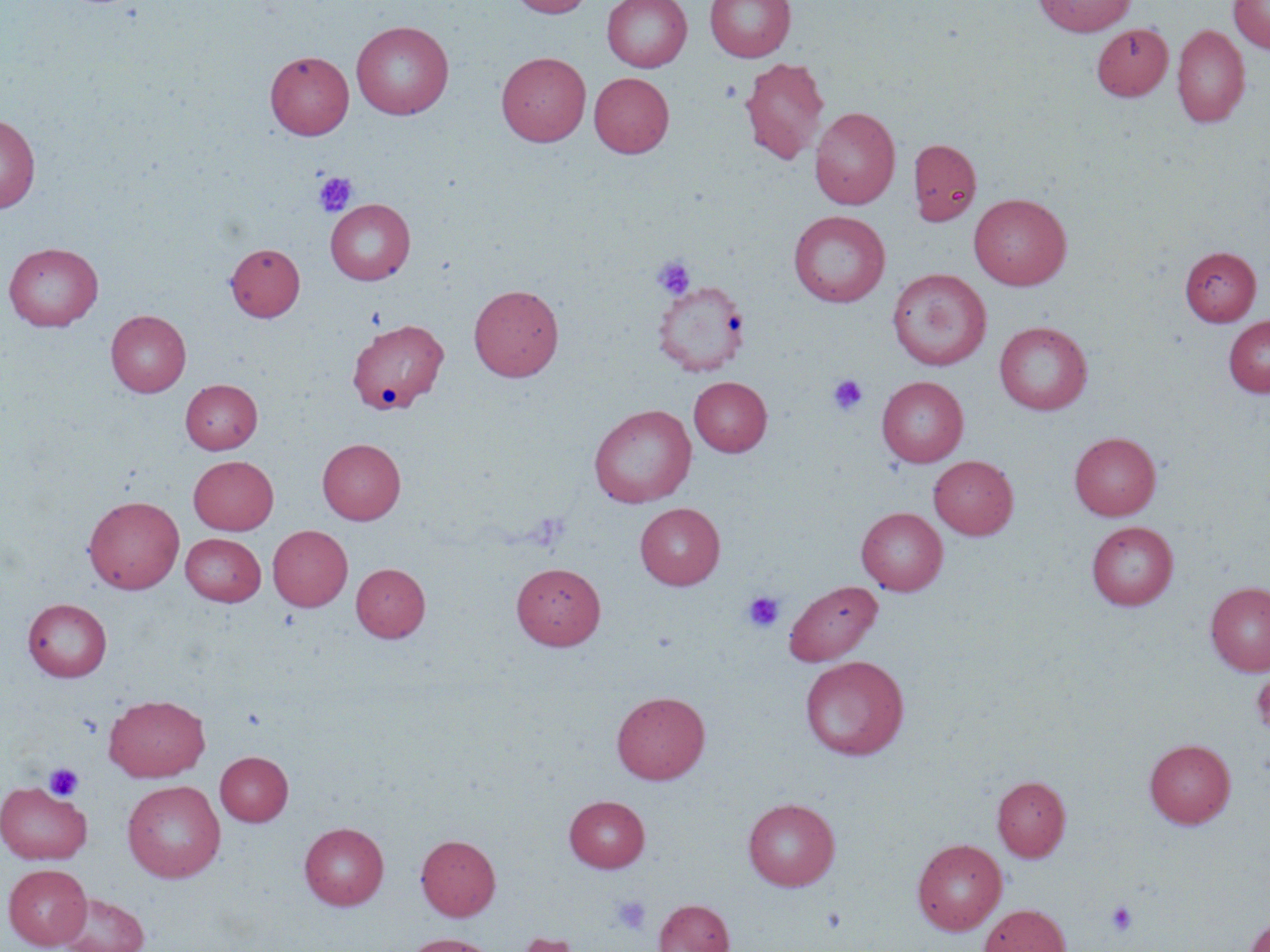

Summary:
  - Coordinate format: approximate bounding boxes as [x1, y1, x2, y2] in pixels
  - Uninfected red blood cell locations: [509, 0, 594, 17], [602, 0, 692, 72], [705, 0, 795, 62], [1035, 0, 1135, 36], [1228, 0, 1270, 53], [351, 20, 454, 118], [1092, 23, 1173, 101], [1172, 25, 1249, 127], [265, 51, 354, 139], [496, 51, 591, 146], [740, 57, 830, 164], [497, 68, 674, 153], [589, 72, 674, 158], [810, 107, 900, 209], [0, 113, 40, 214], [907, 137, 982, 226], [969, 193, 1072, 290], [325, 199, 415, 285], [788, 210, 891, 307], [3, 242, 103, 331], [226, 243, 304, 321], [1180, 246, 1261, 325], [887, 269, 991, 370], [653, 279, 749, 376], [469, 283, 564, 382], [106, 310, 191, 397], [1223, 315, 1270, 398], [995, 321, 1092, 414], [349, 322, 450, 417], [877, 376, 968, 466], [688, 377, 772, 456], [180, 379, 262, 454], [588, 404, 697, 508], [1069, 431, 1161, 520], [317, 438, 406, 524], [188, 455, 278, 534], [929, 455, 1018, 539], [83, 495, 184, 593], [635, 502, 725, 589], [856, 507, 948, 595], [1087, 521, 1177, 610], [267, 525, 352, 611], [181, 533, 266, 606], [351, 562, 430, 642], [512, 562, 606, 649], [783, 580, 882, 666], [1205, 581, 1270, 676], [22, 598, 112, 682], [800, 655, 910, 759], [612, 691, 710, 784], [104, 694, 210, 781], [1144, 739, 1236, 828], [215, 751, 293, 826], [992, 775, 1071, 861], [122, 780, 226, 882], [1, 782, 91, 864], [564, 795, 650, 872], [743, 797, 840, 890], [299, 822, 389, 910], [416, 834, 500, 920], [912, 838, 1007, 935], [3, 863, 92, 950], [57, 892, 149, 952], [654, 899, 734, 952], [979, 904, 1071, 952], [1243, 912, 1270, 952], [513, 932, 584, 952], [403, 934, 498, 952]
  - Platelet locations: [313, 172, 357, 217], [652, 256, 696, 300], [827, 374, 868, 415], [743, 591, 785, 632], [43, 762, 84, 801], [611, 895, 651, 934], [1106, 900, 1138, 936]
  - Slide-level diagnosis: negative for blood parasites
  - Preparation: thin blood film
  - Field of view: single
  - Stain: May-Grünwald-Giemsa
  - Image size: 1270×952 pixels
  - Modality: light microscopy
  - Magnification: 1000x